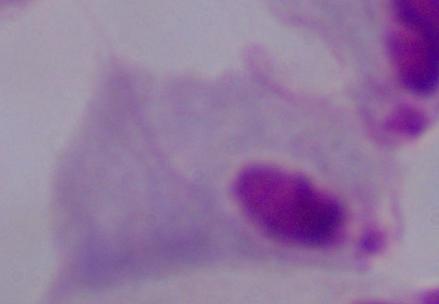

Summary:
  - Identification: trichomonad
  - Modality: photomicrograph
  - Magnification: 1000x